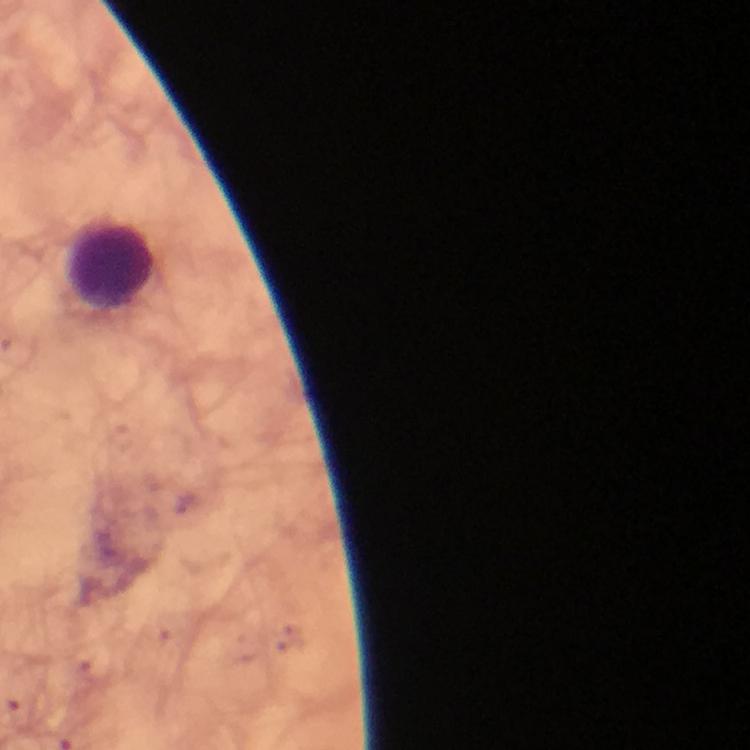
Approximate centers as [x, y] in pixels.
Summary:
  - Leukocyte locations: [114, 264]
  - Capture: smartphone photograph through a microscope
  - Immersion oil: used
  - Image size: 750×750 pixels
  - Stain: Giemsa
  - Plasmodium parasites: none detected
  - Cropped from: one field of view
  - Context: from a diagnostic examination for malaria
  - Magnification: 100x
  - Preparation: thick blood film